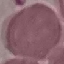

malaria status = uninfected
image type = cell patch, automatically extracted from a larger field of view and resized to 64 × 64 pixels
capture = smartphone camera at the microscope eyepiece
stain = Giemsa
preparation = thin blood smear